Describe the morphology of the red blood cells.
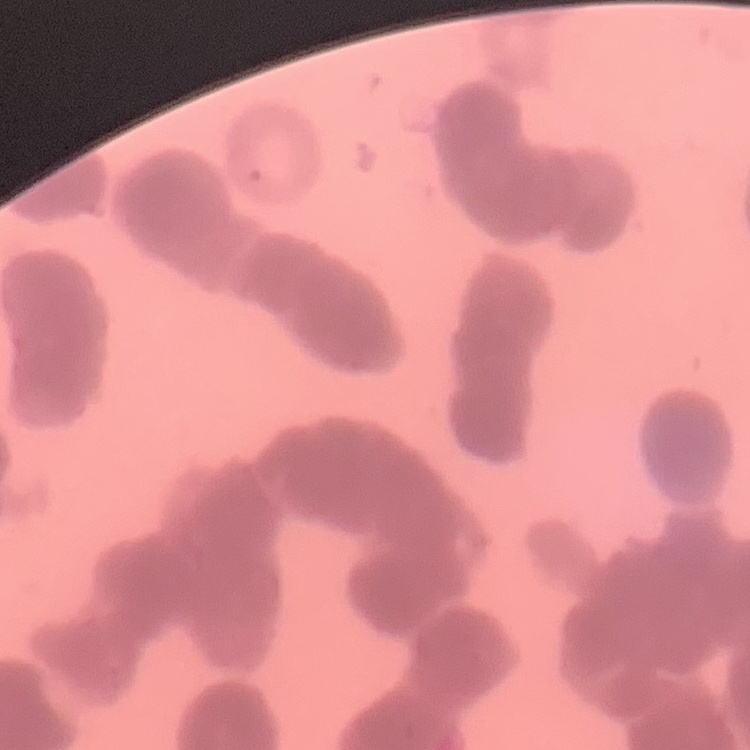

They show rouleaux formation.

Thin blood film. Stained with either Field's or Giemsa. Square crop of a larger photomicrograph.